Assess this cell for malaria.
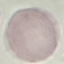

It is uninfected.

Summary:
  - Preparation: thin blood film
  - Capture: smartphone through the microscope eyepiece
  - Stain: Giemsa
  - Image type: automatically extracted cell patch, resized to 64 × 64 pixels